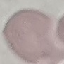
Summary:
  - Result: negative for malaria parasites
  - Image type: automatically extracted cell patch, resized to 64 × 64 pixels
  - Preparation: thin blood film
  - Stain: Giemsa
  - Capture: smartphone camera at the microscope eyepiece